Name the cell type shown.
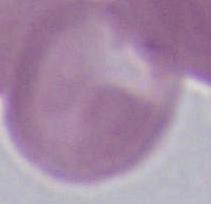

An erythrocyte.

Captured at 1000x magnification. Photomicrograph.